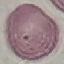

Result: no malaria parasites detected. Thin smear of blood. Automatically extracted cell patch, resized to 64 × 64 pixels. Acquired by smartphone through the microscope eyepiece. Giemsa-stained preparation.